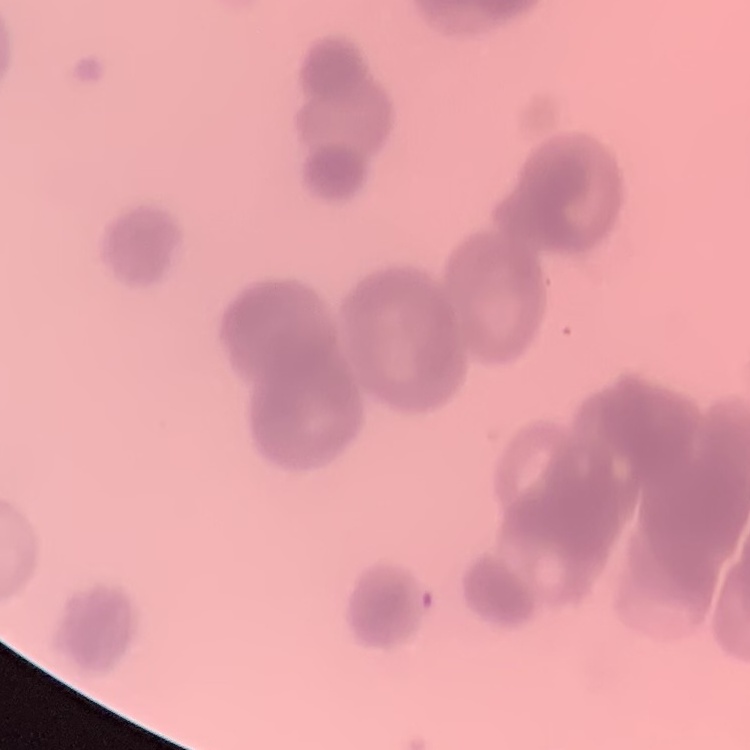 The erythrocytes exhibit rouleaux formation. Thin peripheral smear. Square crop of a larger photomicrograph. Stained with either Field's or Giemsa.